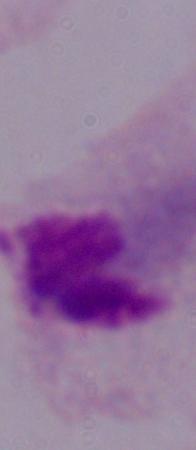 Micrograph. A trichomonad is shown. 1000x magnification.